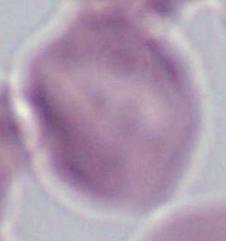
A red blood cell is shown. 1000x magnification. Photomicrograph.